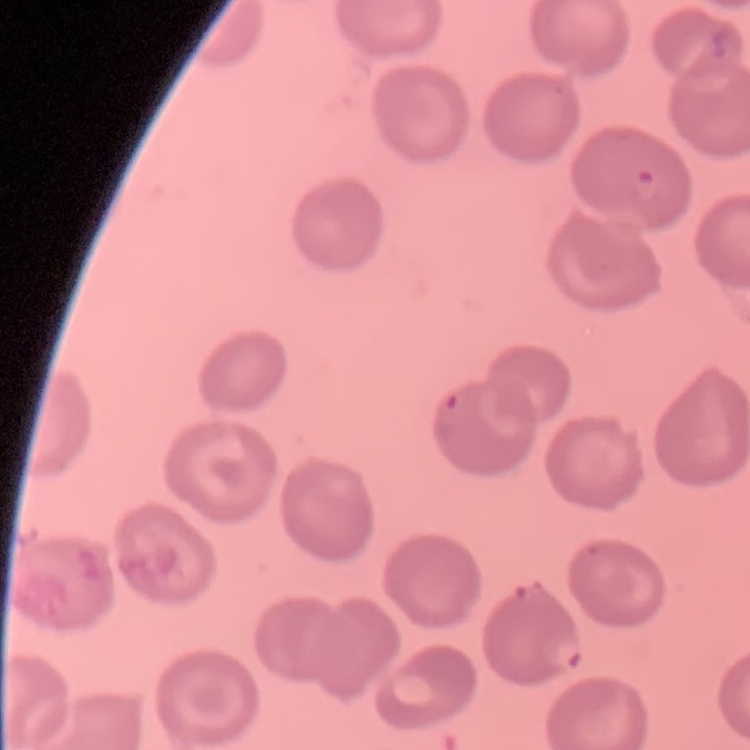
The erythrocytes show no rouleaux formation. Stained with either Field's or Giemsa. One tile cut from a larger photomicrograph. Thin blood smear.